Locate every blood parasite and identify its species.
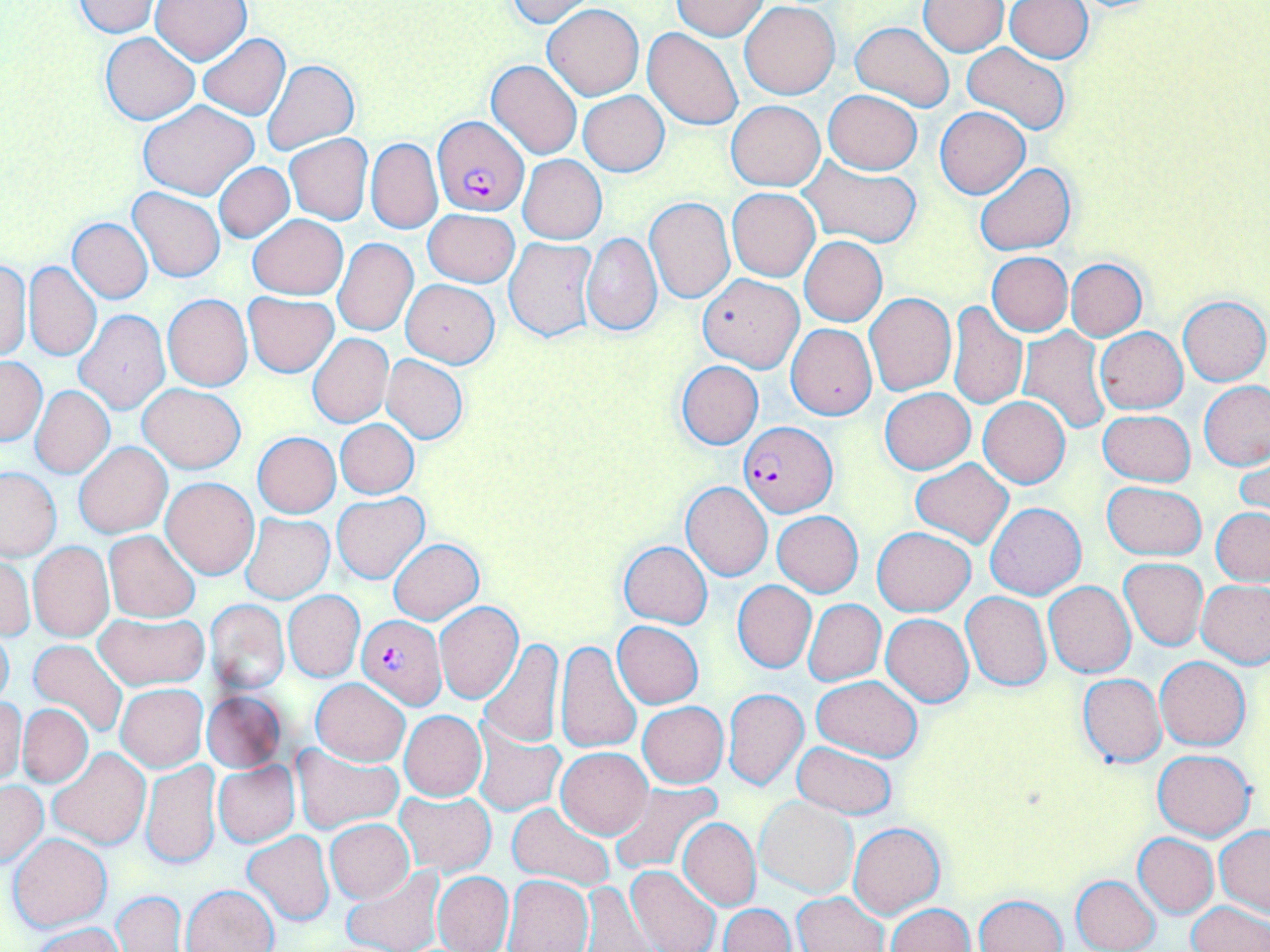
Approximate bounding boxes as (x1,y1)-(x2,y2) corner pairs in pixels.
Plasmodium falciparum-infected red blood cells: (433,117)-(528,216), (739,421)-(836,518), (357,614)-(446,709).
No Plasmodium ovale, Plasmodium malariae, Plasmodium vivax, Babesia divergens, or Trypanosoma brucei observed.

{
  "slide_level_diagnosis": "Plasmodium falciparum",
  "uninfected_red_blood_cell_locations": "approximate bounding boxes as (x1,y1)-(x2,y2) corner pairs in pixels: (150,0)-(251,64), (669,0)-(767,39), (69,1)-(161,37), (504,1)-(596,26), (920,1)-(1008,55), (1005,1)-(1094,62), (740,2)-(840,99), (544,4)-(644,100), (850,21)-(954,112), (643,26)-(743,129), (100,33)-(199,124), (197,34)-(290,120), (962,42)-(1070,137), (263,59)-(358,154), (486,59)-(583,159), (823,89)-(922,174), (579,91)-(669,175), (137,101)-(259,200), (727,101)-(824,191), (934,106)-(1031,199), (285,134)-(372,225), (366,138)-(442,234), (519,154)-(606,244), (798,156)-(922,249), (214,163)-(294,242), (974,163)-(1075,255), (128,186)-(225,283), (727,188)-(820,281), (645,197)-(735,304), (424,209)-(519,287), (247,214)-(347,299), (69,218)-(153,304), (582,232)-(662,336), (800,236)-(887,326), (333,237)-(418,336), (504,238)-(597,343), (986,252)-(1072,336), (0,258)-(31,362), (1066,258)-(1146,340), (24,261)-(101,361), (698,274)-(804,372), (401,279)-(499,367), (243,292)-(339,377), (866,293)-(956,396), (163,295)-(253,391), (1178,296)-(1269,386), (947,301)-(1026,410), (75,310)-(170,413), (787,324)-(876,419), (1017,327)-(1109,436), (1095,327)-(1188,413), (308,334)-(392,427), (382,354)-(468,444), (0,357)-(45,446), (675,360)-(763,450), (1200,380)-(1270,471), (139,383)-(245,473), (31,386)-(114,478), (880,388)-(974,473), (978,396)-(1071,488), (1098,409)-(1195,487), (336,419)-(419,498), (252,432)-(340,517), (74,441)-(172,538), (1235,445)-(1270,526), (910,459)-(1013,548), (1,466)-(63,560), (161,477)-(258,578), (1101,481)-(1207,559), (681,482)-(773,581), (332,493)-(428,583), (985,503)-(1086,600), (1211,507)-(1270,585), (773,511)-(863,596), (242,514)-(333,603), (873,526)-(974,616), (104,530)-(200,623), (388,538)-(483,624), (619,541)-(712,628), (29,542)-(113,641), (1,555)-(33,643), (1119,558)-(1207,650), (1198,579)-(1270,668), (732,581)-(816,673), (1045,581)-(1134,677), (284,591)-(365,681), (961,592)-(1051,691), (205,598)-(289,694), (805,599)-(885,685), (435,602)-(523,703), (93,612)-(208,692), (882,614)-(973,706), (612,620)-(704,707), (0,625)-(15,711), (27,639)-(127,739), (478,639)-(563,749), (554,639)-(641,755), (1155,656)-(1251,750), (1078,672)-(1166,768), (812,676)-(923,761), (310,678)-(409,766), (116,683)-(209,771), (722,687)-(808,792), (202,691)-(285,772), (0,697)-(25,785), (638,702)-(728,788), (17,703)-(93,788), (399,711)-(487,801), (474,721)-(565,816), (791,741)-(897,819), (291,744)-(401,835), (49,747)-(150,849), (555,748)-(651,837), (1152,749)-(1257,842), (140,760)-(223,869), (213,762)-(299,847), (0,779)-(47,868), (609,782)-(720,875), (394,790)-(496,877), (756,798)-(857,898), (508,801)-(614,892), (677,817)-(760,910), (326,819)-(413,902), (848,822)-(944,917), (1216,824)-(1270,918), (243,831)-(335,926), (1133,832)-(1218,918), (8,833)-(111,931), (342,863)-(444,952), (627,864)-(720,952), (432,871)-(514,952), (503,874)-(593,951), (1072,875)-(1160,952), (182,884)-(279,952), (580,884)-(653,951), (113,891)-(185,952), (794,892)-(888,952), (974,894)-(1068,952), (1188,901)-(1268,952), (720,903)-(794,952), (886,903)-(973,952), (31,923)-(123,952)",
  "stain": "May-Grünwald-Giemsa",
  "image_size": "1270×952 pixels",
  "field_of_view": "one of a larger specimen",
  "magnification": "1000x",
  "modality": "optical microscopy",
  "preparation": "thin blood smear"
}